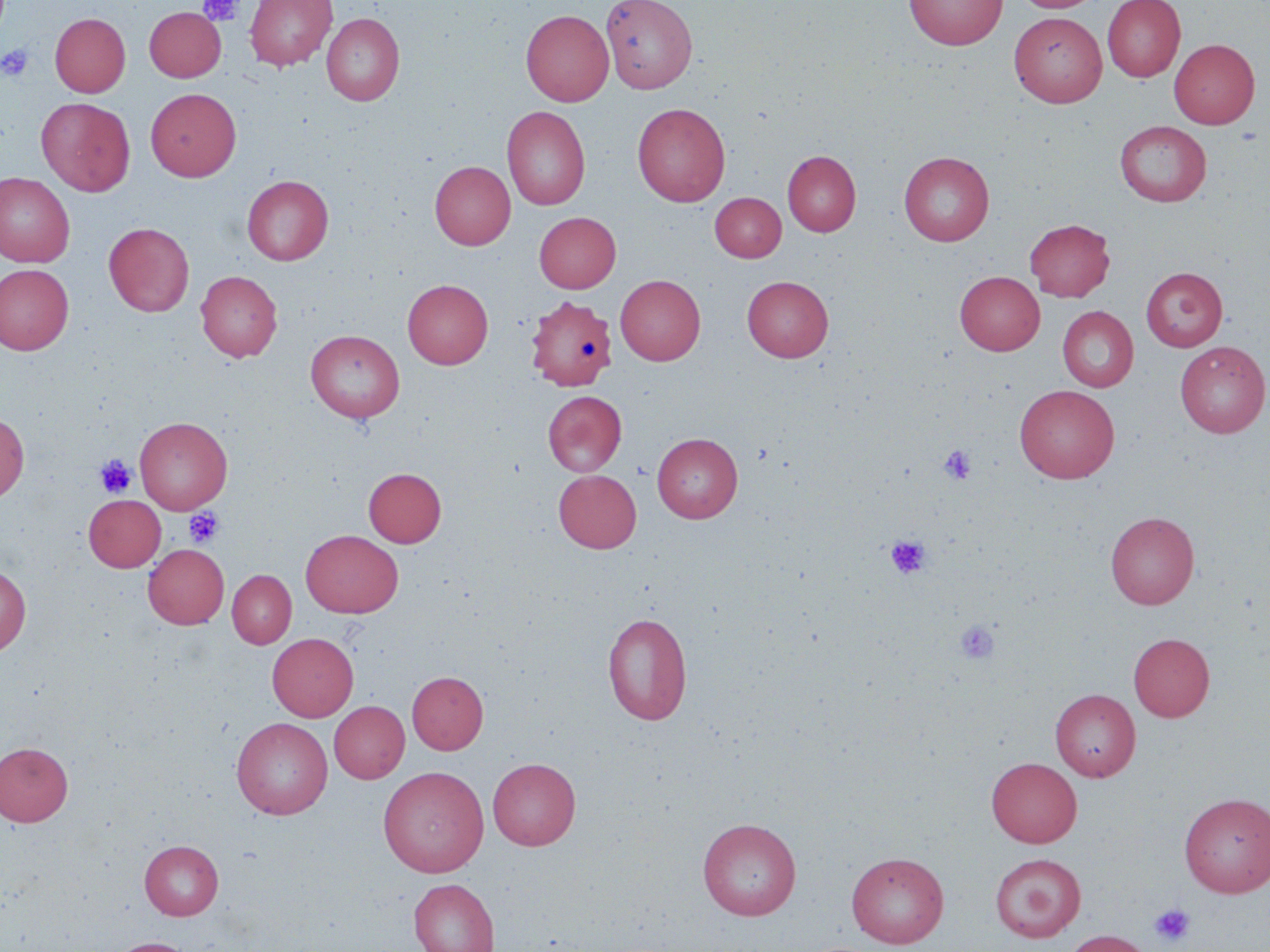

slide_level_diagnosis: no evidence of blood parasites
preparation: thin blood film
platelet_locations: 'approximate bounding boxes as named x1/y1/x2/y2 corners in pixels: (x1=198, y1=0, x2=244, y2=26), (x1=1, y1=44, x2=34, y2=82), (x1=938, y1=444, x2=976, y2=485), (x1=95, y1=454, x2=137, y2=498), (x1=184, y1=507, x2=224, y2=548), (x1=885, y1=534, x2=931, y2=579), (x1=954, y1=619, x2=1000, y2=665), (x1=1150, y1=902, x2=1195, y2=947)'
stain: May-Grünwald-Giemsa
modality: optical microscopy
field_of_view: one of a larger specimen
image_size: 1270×952 pixels
magnification: 1000x
uninfected_red_blood_cell_locations: 'approximate bounding boxes as named x1/y1/x2/y2 corners in pixels: (x1=244, y1=0, x2=336, y2=71), (x1=601, y1=0, x2=697, y2=93), (x1=904, y1=0, x2=1007, y2=49), (x1=1011, y1=0, x2=1102, y2=12), (x1=1102, y1=0, x2=1185, y2=82), (x1=144, y1=6, x2=226, y2=82), (x1=521, y1=9, x2=614, y2=106), (x1=511, y1=10, x2=598, y2=211), (x1=1009, y1=12, x2=1108, y2=108), (x1=49, y1=13, x2=131, y2=97), (x1=321, y1=13, x2=404, y2=106), (x1=1169, y1=38, x2=1260, y2=129), (x1=145, y1=88, x2=241, y2=181), (x1=36, y1=97, x2=135, y2=196), (x1=632, y1=102, x2=731, y2=207), (x1=502, y1=106, x2=590, y2=210), (x1=1115, y1=120, x2=1211, y2=207), (x1=783, y1=150, x2=861, y2=236), (x1=899, y1=151, x2=995, y2=246), (x1=430, y1=160, x2=515, y2=250), (x1=0, y1=172, x2=75, y2=267), (x1=242, y1=175, x2=333, y2=264), (x1=710, y1=192, x2=786, y2=261), (x1=534, y1=212, x2=621, y2=293), (x1=1024, y1=219, x2=1115, y2=302), (x1=104, y1=222, x2=194, y2=317), (x1=0, y1=264, x2=74, y2=355), (x1=1140, y1=267, x2=1227, y2=351), (x1=196, y1=271, x2=282, y2=361), (x1=955, y1=271, x2=1045, y2=355), (x1=615, y1=275, x2=705, y2=365), (x1=742, y1=275, x2=833, y2=362), (x1=402, y1=279, x2=493, y2=369), (x1=525, y1=295, x2=617, y2=391), (x1=1058, y1=306, x2=1138, y2=391), (x1=306, y1=330, x2=404, y2=422), (x1=1175, y1=342, x2=1269, y2=438), (x1=1014, y1=384, x2=1119, y2=483), (x1=543, y1=390, x2=627, y2=476), (x1=0, y1=412, x2=29, y2=502), (x1=135, y1=416, x2=232, y2=514), (x1=651, y1=432, x2=743, y2=522), (x1=363, y1=467, x2=446, y2=547), (x1=553, y1=469, x2=642, y2=552), (x1=84, y1=494, x2=165, y2=572), (x1=1105, y1=511, x2=1199, y2=609), (x1=300, y1=530, x2=403, y2=617), (x1=143, y1=544, x2=228, y2=627), (x1=0, y1=564, x2=31, y2=656), (x1=228, y1=570, x2=296, y2=648), (x1=602, y1=612, x2=692, y2=725), (x1=267, y1=633, x2=358, y2=721), (x1=1128, y1=633, x2=1214, y2=721), (x1=407, y1=671, x2=488, y2=754), (x1=1051, y1=689, x2=1141, y2=781), (x1=329, y1=701, x2=409, y2=783), (x1=231, y1=717, x2=332, y2=818), (x1=0, y1=742, x2=73, y2=826), (x1=986, y1=757, x2=1082, y2=847), (x1=488, y1=758, x2=581, y2=850), (x1=378, y1=766, x2=489, y2=878), (x1=1179, y1=792, x2=1270, y2=897), (x1=697, y1=817, x2=802, y2=920), (x1=139, y1=839, x2=223, y2=920), (x1=846, y1=852, x2=949, y2=948), (x1=989, y1=853, x2=1086, y2=942), (x1=409, y1=878, x2=499, y2=952), (x1=1063, y1=930, x2=1153, y2=952), (x1=108, y1=937, x2=196, y2=952)'